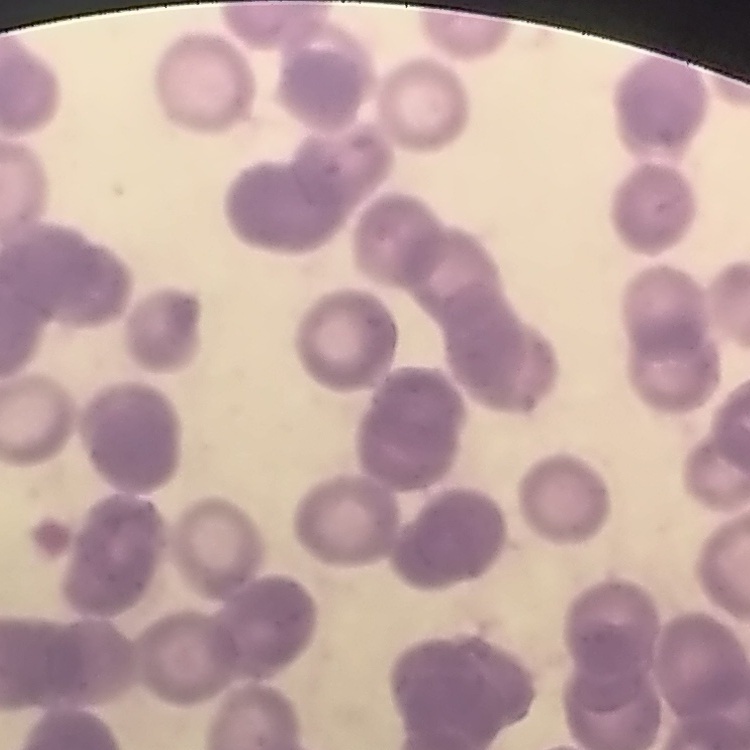

The red blood cells exhibit rouleaux formation. One tile cut from a larger photomicrograph. Thin blood smear. Field's or Giemsa stain.